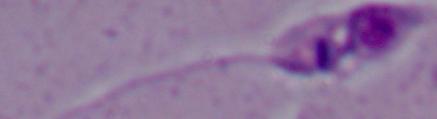

modality = photomicrograph
identification = Leishmania
magnification = 1000x